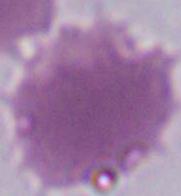
Photomicrograph. 1000x magnification. An erythrocyte is shown.